Describe the morphology of the red blood cells.
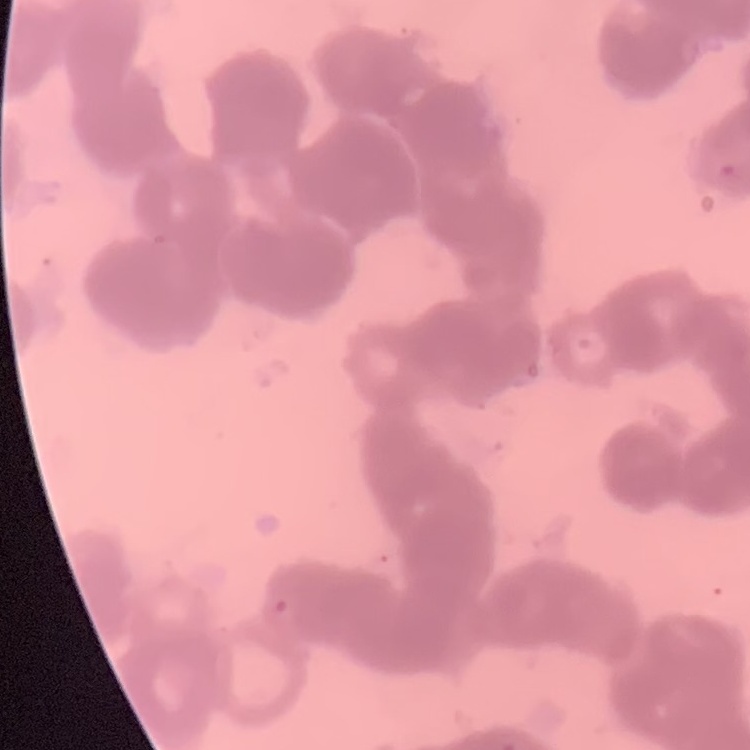

They show rouleaux formation.

Summary:
  - Image type: one tile cut from a larger photomicrograph
  - Stain: Field's or Giemsa
  - Preparation: thin peripheral smear